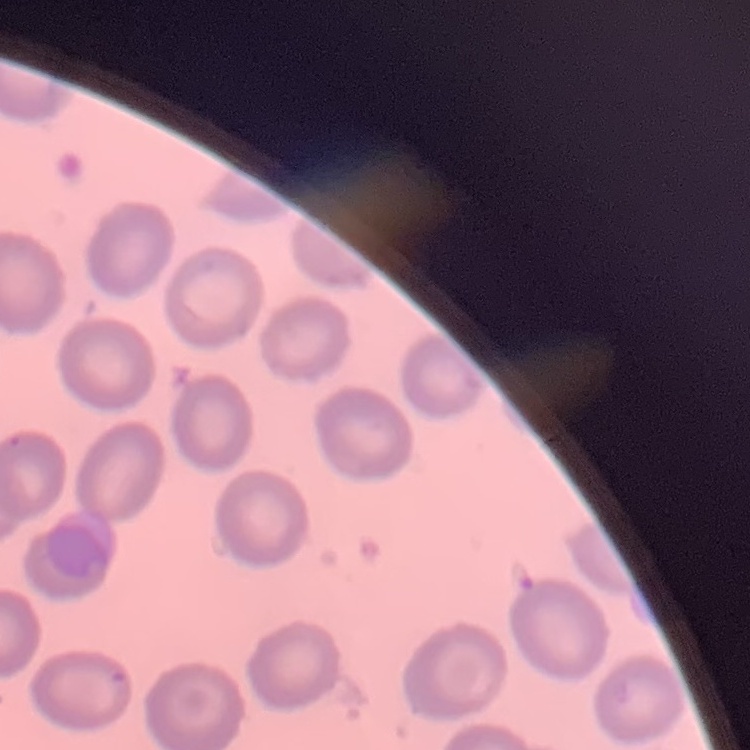

Summary:
  - Red blood cell morphology: no rouleaux formation
  - Stain: Field's or Giemsa
  - Image type: square crop of a larger photomicrograph
  - Preparation: thin peripheral smear